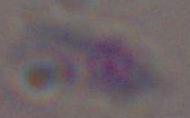 Toxoplasma gondii is seen. 1000x magnification. Photomicrograph.